Assess this cell for malaria.
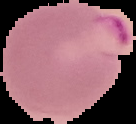
It is parasitized.

{
  "preparation": "thin blood smear",
  "image_size": "136×124 pixels",
  "image_type": "segmented cell region with the area outside set to black"
}